Name the parasite shown.
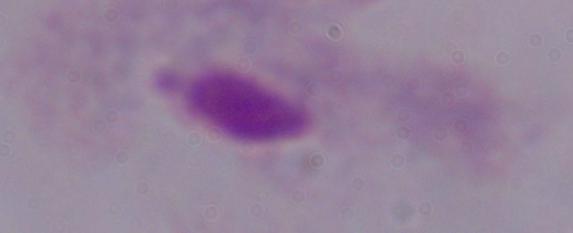
This is a trichomonad.

Micrograph. Captured at 1000x magnification.